Rate the background quality.
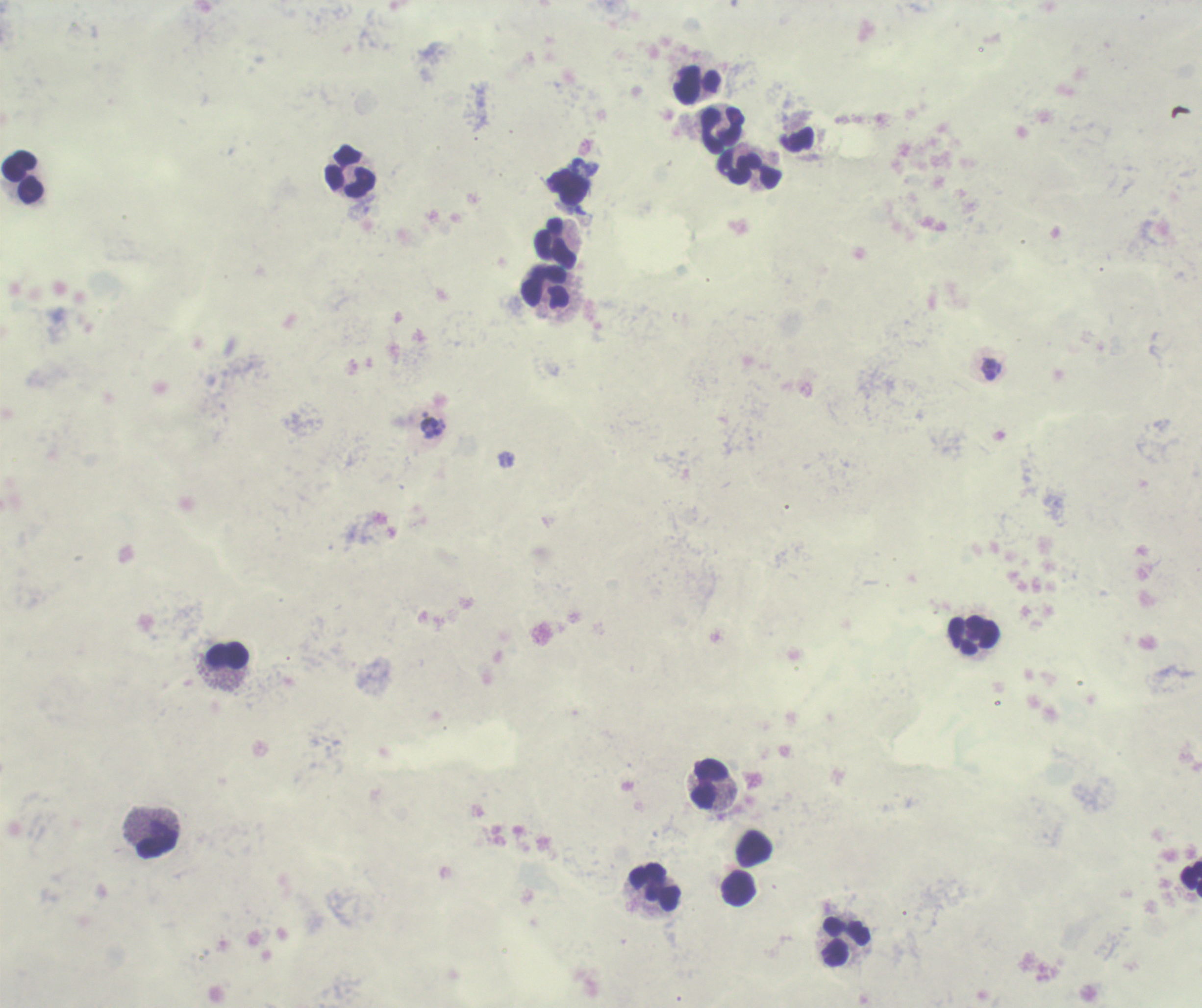

Poor.

{
  "result": "positive for malaria parasites",
  "stain": "Romanowsky",
  "leukocyte_locations": "approximate object centers, in pixels from the top-left corner: (x=697, y=84), (x=723, y=130), (x=750, y=169), (x=350, y=172), (x=23, y=177), (x=556, y=242), (x=546, y=287), (x=975, y=635), (x=227, y=655), (x=710, y=784), (x=158, y=843), (x=754, y=848), (x=1191, y=878), (x=655, y=887), (x=739, y=888), (x=847, y=941)",
  "coloration_quality": "bad",
  "preparation": "thick blood film",
  "trophozoite_locations": "approximate object centers, in pixels from the top-left corner: (x=991, y=369)",
  "image_size": "1202×1008 pixels",
  "field_of_view": "one from this slide",
  "context": "previously used in a real diagnosis",
  "magnification": "100x"
}